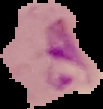
Summary:
  - Result: Plasmodium parasites detected
  - Image size: 103×109 pixels
  - Image type: cell region segmented out of the field of view; surrounding area masked to black
  - Preparation: thin blood smear